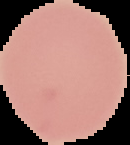

Cell region segmented out of the field of view; the surrounding area is masked to black. Image is 130×145 pixels. Result: no Plasmodium parasites detected. From a thin blood smear.